Describe the morphology of the erythrocytes.
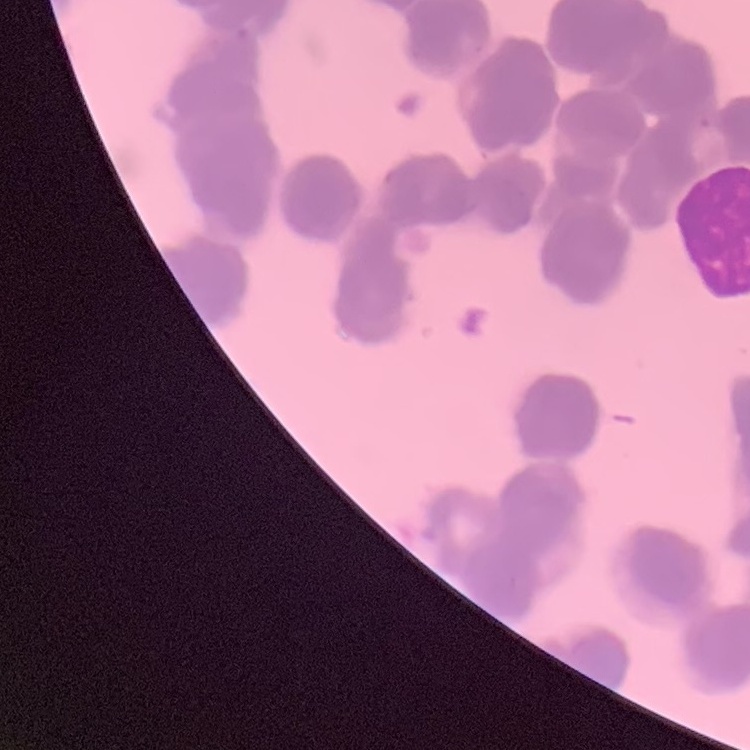

They show rouleaux formation.

Summary:
  - Preparation: thin peripheral smear
  - Image type: one tile cut from a larger photomicrograph
  - Stain: Field's or Giemsa